Name the cell type shown.
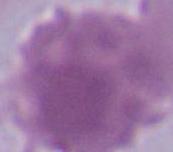
An erythrocyte.

Photomicrograph. Captured at 1000x magnification.